Comment on the morphology of the red blood cells.
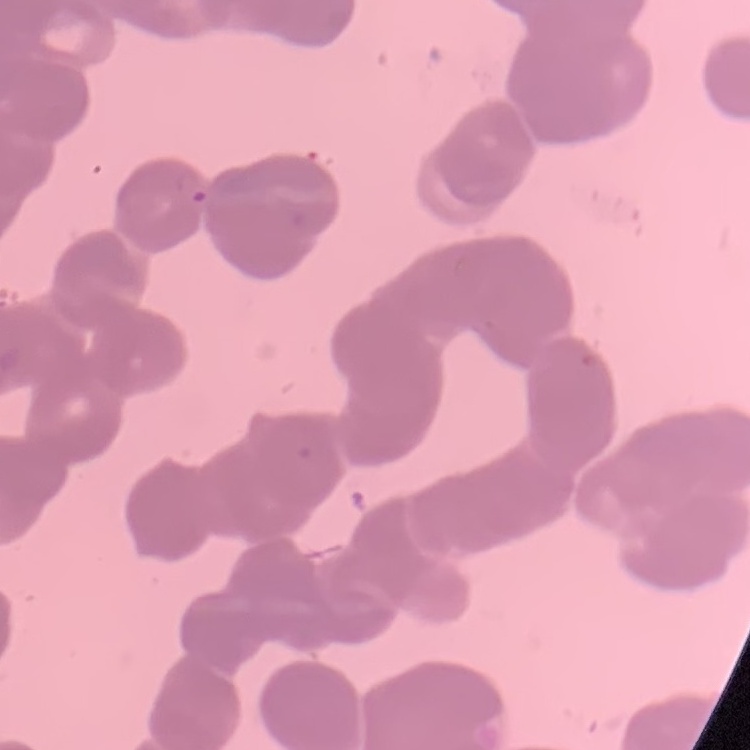
They show rouleaux formation.

Summary:
  - Image type: one tile cut from a larger photomicrograph
  - Stain: Field's or Giemsa
  - Preparation: thin blood film